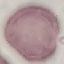

result = no malaria parasites detected
preparation = thin blood smear
stain = Giemsa
capture = smartphone camera at the microscope eyepiece
image type = automatically extracted cell patch, resized to 64 × 64 pixels